State the blood parasite species.
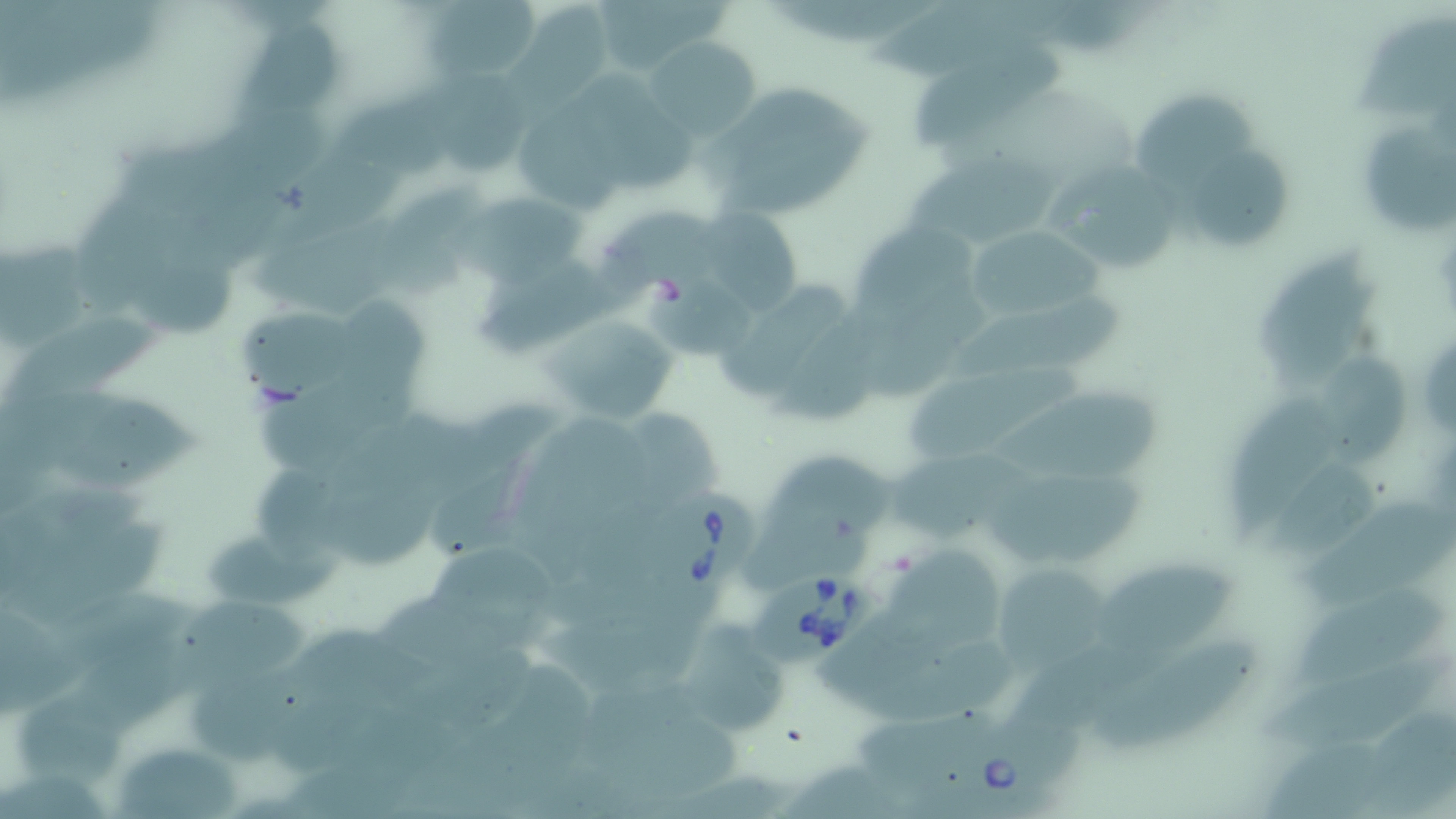
Babesia divergens.

Summary:
  - Coordinate format: approximate bounding boxes as named x1/y1/x2/y2 corners in pixels
  - Babesia divergens-infected red blood cell locations: (x1=653, y1=484, x2=765, y2=595), (x1=749, y1=566, x2=877, y2=666), (x1=926, y1=711, x2=1076, y2=819)
  - Uninfected red blood cell locations: (x1=423, y1=0, x2=538, y2=86), (x1=865, y1=0, x2=1051, y2=87), (x1=514, y1=5, x2=616, y2=101), (x1=1352, y1=13, x2=1453, y2=115), (x1=233, y1=23, x2=344, y2=120), (x1=647, y1=37, x2=762, y2=140), (x1=904, y1=48, x2=1065, y2=152), (x1=426, y1=74, x2=543, y2=182), (x1=710, y1=81, x2=872, y2=217), (x1=1141, y1=93, x2=1263, y2=194), (x1=515, y1=107, x2=629, y2=215), (x1=1364, y1=122, x2=1452, y2=234), (x1=1185, y1=141, x2=1288, y2=249), (x1=904, y1=157, x2=1077, y2=259), (x1=1053, y1=165, x2=1185, y2=272), (x1=375, y1=184, x2=494, y2=301), (x1=441, y1=186, x2=599, y2=285), (x1=691, y1=191, x2=808, y2=316), (x1=964, y1=223, x2=1103, y2=327), (x1=131, y1=234, x2=239, y2=343), (x1=1253, y1=248, x2=1377, y2=386), (x1=715, y1=280, x2=849, y2=408), (x1=232, y1=298, x2=379, y2=398), (x1=944, y1=300, x2=1135, y2=379), (x1=772, y1=311, x2=882, y2=430), (x1=543, y1=312, x2=680, y2=427), (x1=3, y1=317, x2=166, y2=400), (x1=1415, y1=325, x2=1456, y2=446), (x1=906, y1=368, x2=1085, y2=461), (x1=7, y1=390, x2=210, y2=491), (x1=998, y1=390, x2=1166, y2=486), (x1=1222, y1=392, x2=1337, y2=543), (x1=887, y1=449, x2=1035, y2=541), (x1=986, y1=468, x2=1149, y2=563), (x1=1291, y1=493, x2=1453, y2=613), (x1=205, y1=530, x2=345, y2=611), (x1=427, y1=540, x2=559, y2=649), (x1=888, y1=555, x2=1010, y2=660), (x1=1106, y1=556, x2=1240, y2=674), (x1=989, y1=559, x2=1114, y2=674), (x1=1291, y1=589, x2=1447, y2=692), (x1=176, y1=596, x2=316, y2=698), (x1=685, y1=613, x2=787, y2=732), (x1=1097, y1=645, x2=1257, y2=753), (x1=19, y1=692, x2=131, y2=798), (x1=116, y1=744, x2=245, y2=819)
  - Stain: May-Grünwald-Giemsa
  - Image size: 1456×819 pixels
  - Magnification: 1000x
  - Modality: optical microscopy
  - Field of view: one of a larger specimen
  - Preparation: thin blood film